Give the position of every malaria parasite.
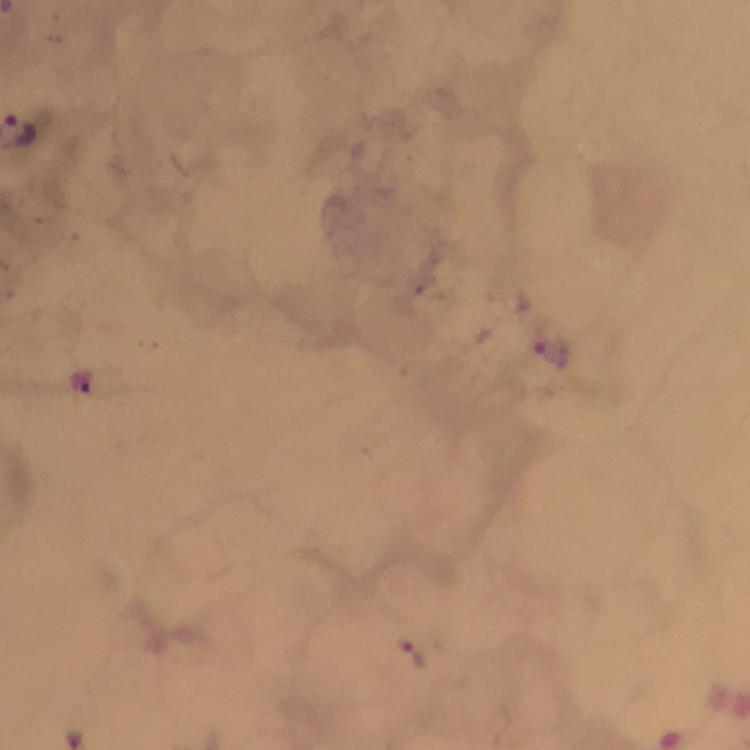
Approximate centers as {x, y} in pixels.
Malaria parasites: {553, 354}, {416, 654}.

From a diagnostic examination for malaria. 100x magnification. Photographed through the microscope with a smartphone camera. Giemsa stain. Immersion oil was used. Thick smear. Image is 750×750 pixels. A crop from one field of view.